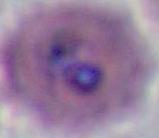

Photomicrograph. A Plasmodium parasite is seen. Captured at either 400x or 1000x magnification.